Name the cell type shown.
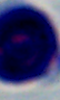
This is a leukocyte.

Summary:
  - Magnification: 1000x
  - Modality: photomicrograph